Assess the morphology of the red blood cells.
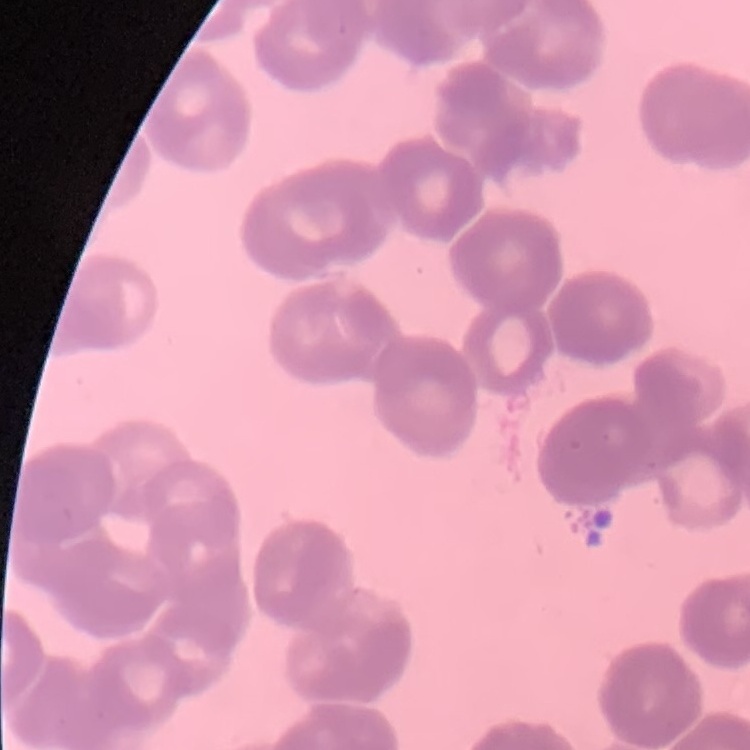
They show rouleaux formation.

Summary:
  - Preparation: thin blood film
  - Stain: Field's or Giemsa
  - Image type: square crop of a larger photomicrograph